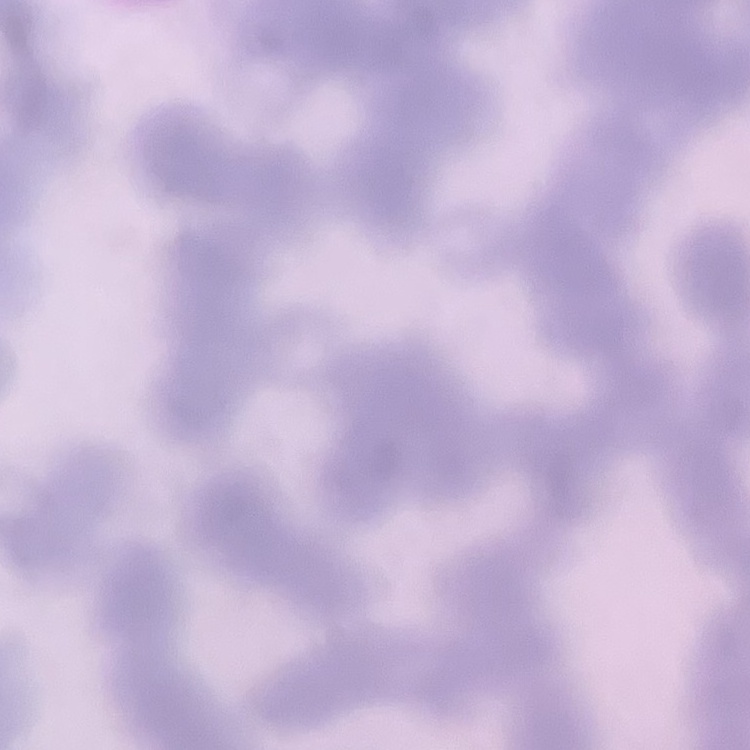
The erythrocytes exhibit rouleaux formation. Stained with either Field's or Giemsa. Thin peripheral smear. Square crop of a larger photomicrograph.